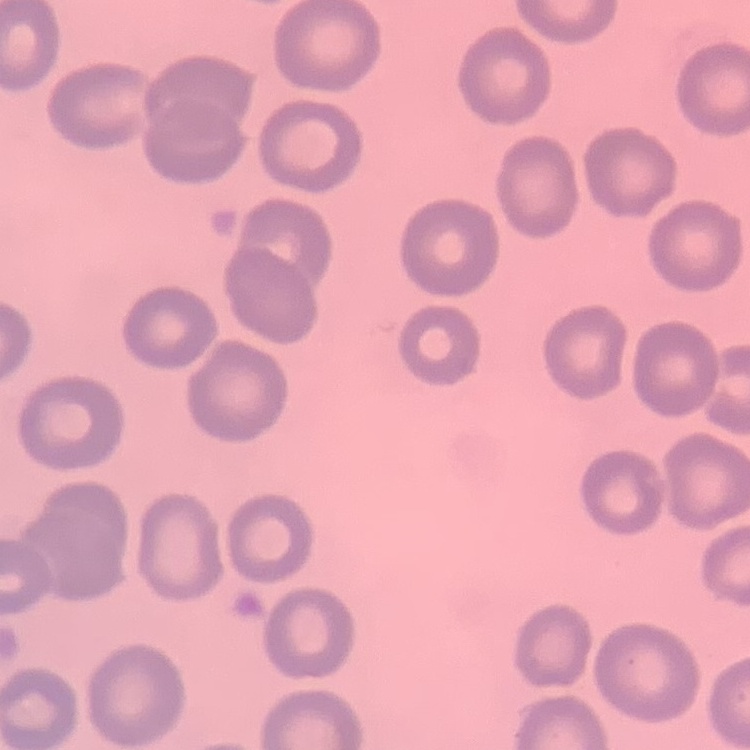

erythrocyte morphology = no rouleaux formation
preparation = thin blood film
stain = Field's or Giemsa
image type = square crop of a larger photomicrograph